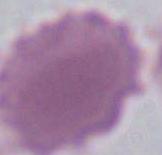

Summary:
  - Magnification: 1000x
  - Identification: red blood cell
  - Modality: micrograph